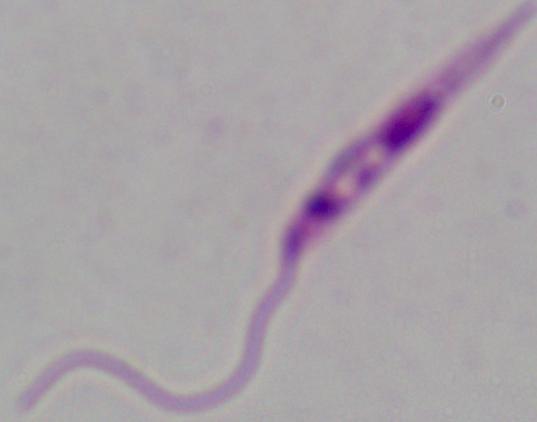
magnification: 1000x
modality: micrograph
identification: Leishmania